Report the malaria status of this cell.
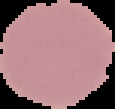
It is uninfected.

Summary:
  - Preparation: thin blood smear
  - Image size: 115×109 pixels
  - Image type: segmented cell region on a black background